Assess the morphology of the erythrocytes.
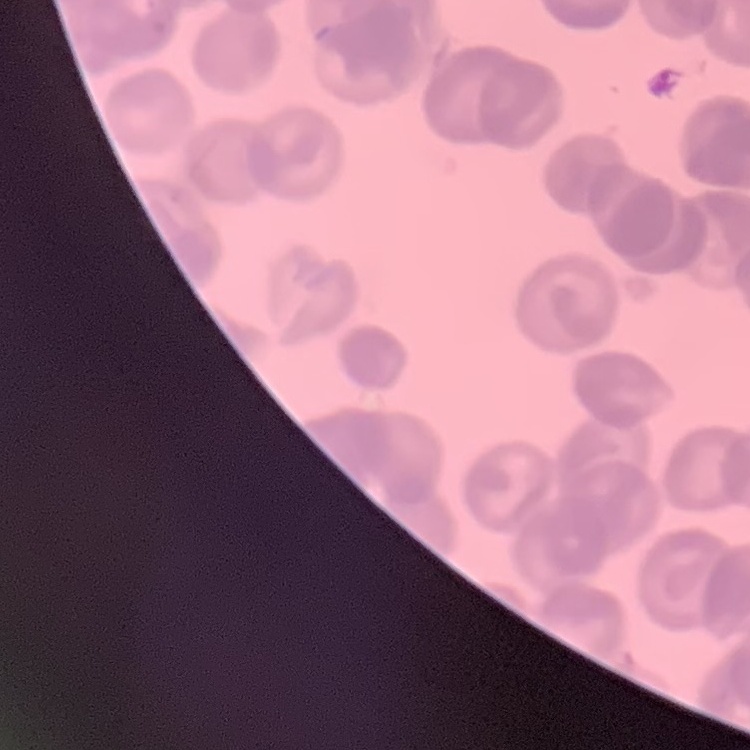

They show rouleaux formation.

image type = one tile cut from a larger photomicrograph
stain = Field's or Giemsa
preparation = thin peripheral smear